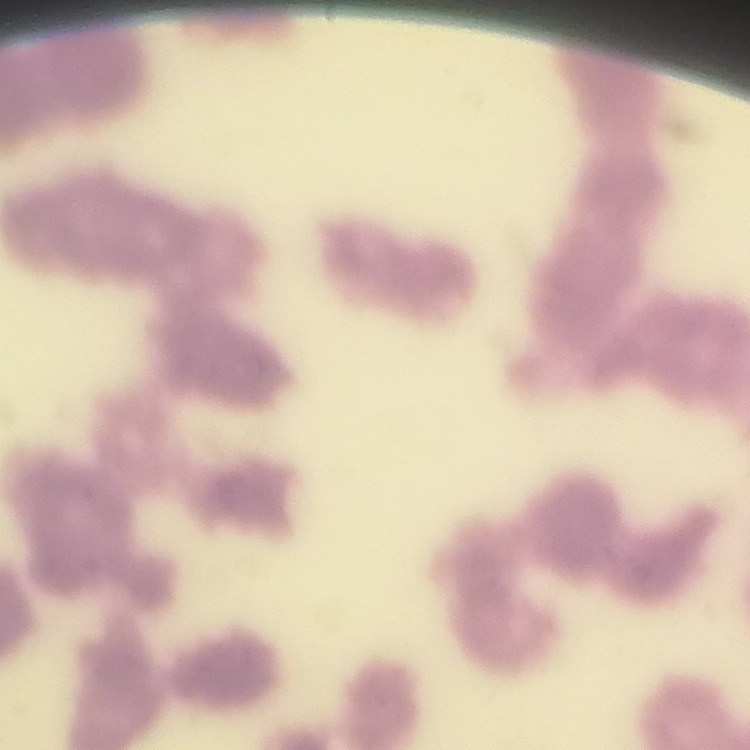

{
  "red_blood_cell_morphology": "rouleaux formation",
  "stain": "Field's or Giemsa",
  "preparation": "thin blood smear",
  "image_type": "square crop of a larger photomicrograph"
}